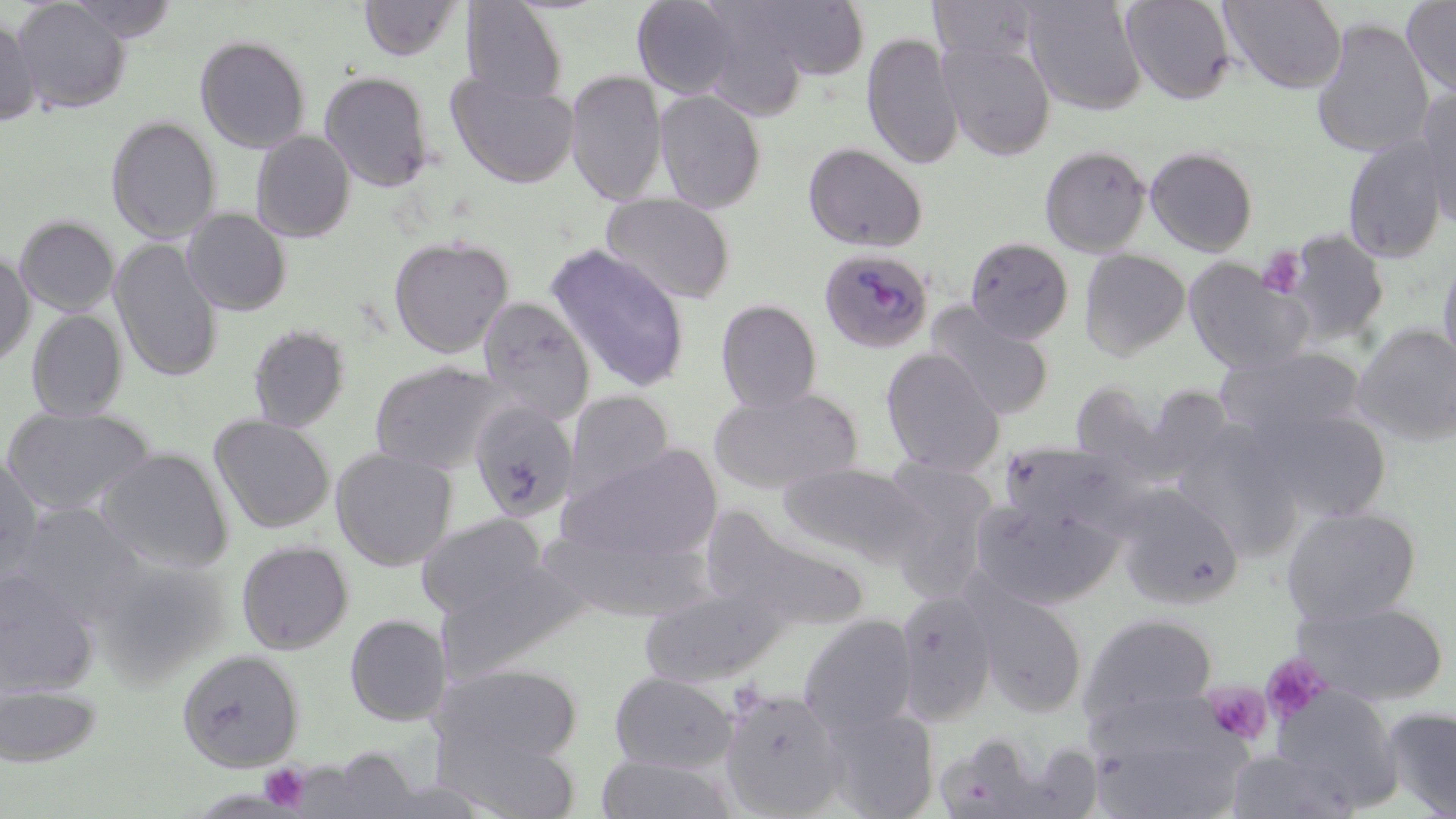
slide_level_diagnosis: Plasmodium malariae
magnification: 1000x
plasmodium_malariae_infected_red_blood_cell_locations: 'approximate bounding boxes as (x1,y1)-(x2,y2) corner pairs in pixels: (819,248)-(933,353)'
stain: May-Grünwald-Giemsa
preparation: thin blood film
modality: optical microscopy
platelet_locations: 'approximate bounding boxes as (x1,y1)-(x2,y2) corner pairs in pixels: (1256,247)-(1306,299), (1261,655)-(1330,724), (1205,683)-(1273,745), (260,763)-(310,812)'
image_size: 1456×819 pixels
uninfected_red_blood_cell_locations: 'approximate bounding boxes as (x1,y1)-(x2,y2) corner pairs in pixels: (12,0)-(131,114), (64,0)-(181,42), (358,0)-(464,61), (633,0)-(740,99), (736,0)-(873,80), (930,0)-(1040,65), (1022,0)-(1148,115), (1121,0)-(1236,103), (1219,0)-(1348,93), (1401,0)-(1456,99), (461,1)-(568,106), (695,6)-(815,121), (0,17)-(40,126), (1311,18)-(1434,158), (862,33)-(963,171), (194,35)-(312,153), (939,40)-(1056,159), (565,69)-(667,205), (320,70)-(435,193), (446,72)-(579,188), (1415,88)-(1456,230), (655,89)-(767,213), (106,115)-(221,244), (251,131)-(356,243), (1343,137)-(1450,264), (803,141)-(928,253), (1040,145)-(1151,257), (1145,146)-(1259,256), (600,192)-(735,306), (182,208)-(292,316), (14,215)-(120,317), (1285,229)-(1390,343), (389,236)-(514,358), (964,237)-(1074,344), (109,238)-(223,382), (546,244)-(691,393), (1079,249)-(1191,359), (0,250)-(35,367), (1438,251)-(1456,376), (1183,257)-(1311,373), (477,296)-(596,423), (715,298)-(823,412), (927,303)-(1054,419), (26,309)-(128,421), (247,323)-(351,432), (1353,323)-(1456,446), (881,347)-(1005,476), (1218,347)-(1366,440), (368,360)-(515,473), (1143,383)-(1239,479), (709,387)-(863,493), (563,389)-(675,503), (468,399)-(579,523), (0,405)-(157,515), (1251,406)-(1391,522), (209,415)-(335,533), (1171,422)-(1301,555), (1000,442)-(1130,534), (558,444)-(723,564), (96,447)-(234,572), (331,447)-(458,570), (0,454)-(44,579), (877,459)-(999,592), (778,461)-(927,565), (1114,485)-(1244,608), (973,497)-(1123,608), (14,503)-(145,618), (1281,506)-(1422,624), (703,509)-(871,635), (416,513)-(548,619), (540,528)-(715,620), (236,540)-(354,655), (88,554)-(227,687), (436,558)-(589,679), (0,568)-(98,696), (640,583)-(791,687), (971,587)-(1089,716), (894,589)-(998,722), (1294,599)-(1449,704), (1081,613)-(1218,727), (345,614)-(451,726), (798,614)-(918,733), (177,649)-(304,771), (437,664)-(584,769), (609,671)-(739,773), (0,683)-(102,766), (719,687)-(848,817), (1270,689)-(1402,810), (821,707)-(940,818), (1382,707)-(1456,817), (1093,717)-(1250,817), (438,724)-(583,818), (933,733)-(1065,818), (313,748)-(425,816), (1227,750)-(1354,817), (596,754)-(739,818)'
field_of_view: one of a larger specimen